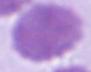

identification: erythrocyte
modality: photomicrograph
magnification: 1000x